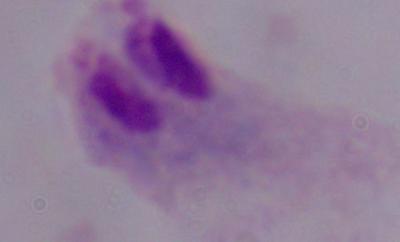
magnification = 1000x
modality = photomicrograph
identification = trichomonad